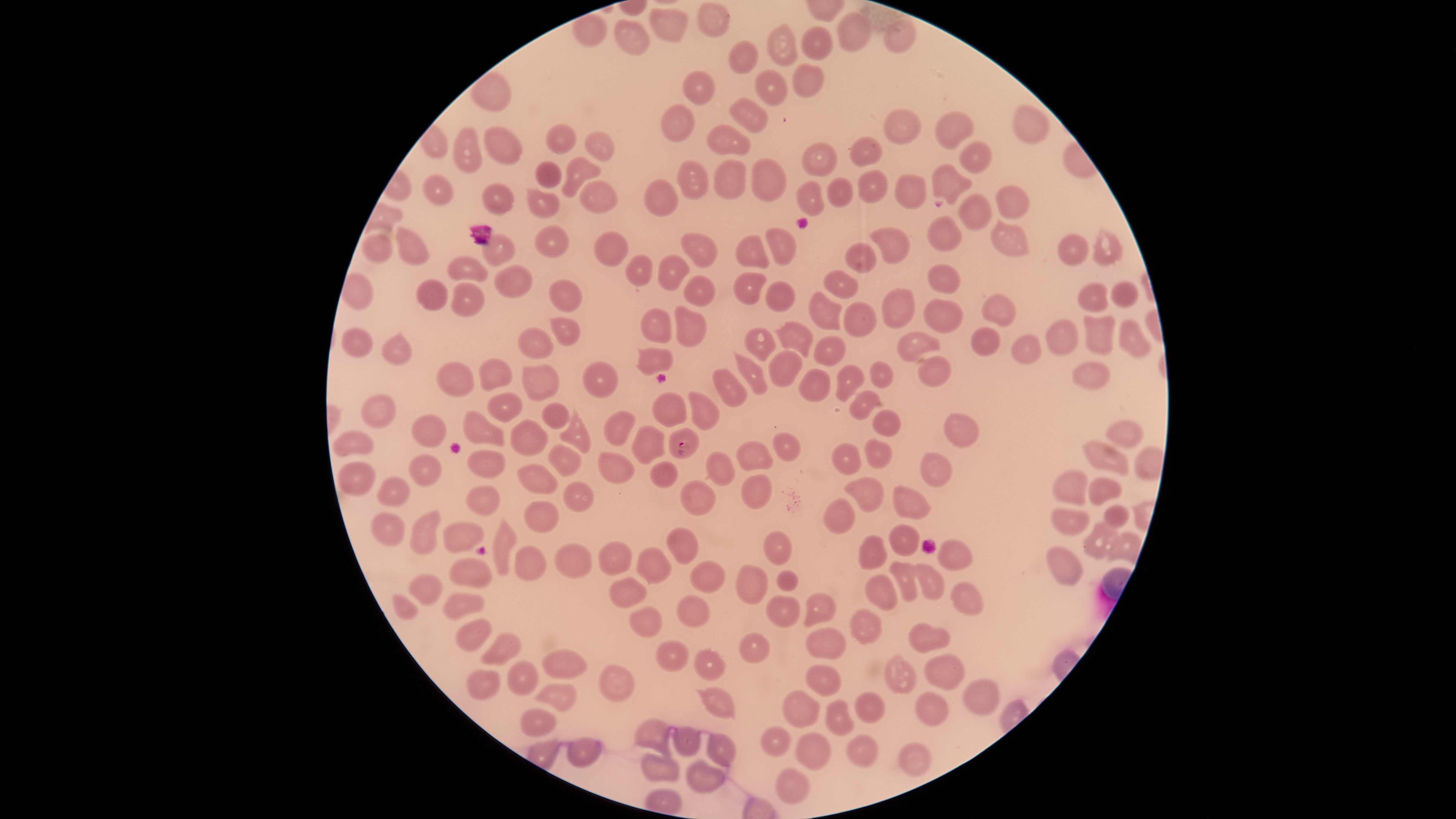

Approximate bounding boxes, in pixels from the top-left corner.
Summary:
  - Uninfected red blood cells: (left=696, top=1, right=732, bottom=41), (left=648, top=6, right=688, bottom=44), (left=835, top=11, right=872, bottom=52), (left=614, top=16, right=651, bottom=57), (left=882, top=18, right=917, bottom=55), (left=765, top=23, right=799, bottom=69), (left=801, top=23, right=833, bottom=61), (left=728, top=40, right=760, bottom=74), (left=792, top=63, right=825, bottom=98), (left=754, top=68, right=788, bottom=106), (left=683, top=70, right=716, bottom=105), (left=728, top=96, right=769, bottom=133), (left=660, top=103, right=695, bottom=143), (left=1010, top=103, right=1051, bottom=146), (left=882, top=108, right=922, bottom=146), (left=934, top=109, right=975, bottom=151), (left=545, top=122, right=577, bottom=156), (left=706, top=122, right=751, bottom=157), (left=483, top=126, right=524, bottom=167), (left=453, top=127, right=483, bottom=174), (left=583, top=128, right=616, bottom=164), (left=849, top=136, right=883, bottom=166), (left=959, top=140, right=993, bottom=175), (left=801, top=143, right=839, bottom=179), (left=561, top=155, right=602, bottom=199), (left=750, top=158, right=788, bottom=204), (left=712, top=159, right=748, bottom=200), (left=534, top=160, right=563, bottom=188), (left=676, top=160, right=709, bottom=201), (left=930, top=162, right=974, bottom=206), (left=857, top=169, right=889, bottom=203), (left=422, top=173, right=454, bottom=207), (left=895, top=173, right=927, bottom=210), (left=826, top=176, right=854, bottom=207), (left=644, top=178, right=679, bottom=217), (left=579, top=180, right=619, bottom=214), (left=795, top=180, right=824, bottom=217), (left=481, top=182, right=516, bottom=217), (left=995, top=184, right=1030, bottom=221), (left=524, top=186, right=561, bottom=218), (left=957, top=193, right=993, bottom=232), (left=927, top=216, right=963, bottom=253), (left=990, top=218, right=1031, bottom=259), (left=394, top=224, right=431, bottom=267), (left=534, top=224, right=570, bottom=259), (left=765, top=226, right=798, bottom=267), (left=869, top=226, right=910, bottom=266), (left=1092, top=227, right=1121, bottom=266), (left=593, top=230, right=630, bottom=267), (left=362, top=232, right=394, bottom=266), (left=681, top=232, right=718, bottom=269), (left=1057, top=232, right=1090, bottom=267), (left=480, top=234, right=517, bottom=267), (left=734, top=234, right=769, bottom=269), (left=843, top=242, right=878, bottom=274), (left=447, top=254, right=488, bottom=283), (left=625, top=254, right=654, bottom=288), (left=657, top=254, right=690, bottom=292), (left=493, top=263, right=533, bottom=299), (left=927, top=263, right=962, bottom=296), (left=732, top=270, right=768, bottom=305), (left=822, top=270, right=859, bottom=300), (left=683, top=274, right=716, bottom=307), (left=416, top=276, right=450, bottom=312), (left=549, top=279, right=584, bottom=313), (left=450, top=280, right=486, bottom=319), (left=765, top=280, right=797, bottom=312), (left=1110, top=280, right=1139, bottom=308), (left=1077, top=282, right=1108, bottom=314), (left=881, top=287, right=916, bottom=328), (left=808, top=290, right=842, bottom=331), (left=980, top=292, right=1016, bottom=328), (left=923, top=299, right=963, bottom=334), (left=843, top=301, right=877, bottom=339), (left=674, top=304, right=708, bottom=348), (left=639, top=306, right=673, bottom=344), (left=1082, top=313, right=1117, bottom=358), (left=548, top=316, right=581, bottom=348), (left=1045, top=318, right=1079, bottom=356), (left=1117, top=318, right=1152, bottom=360), (left=772, top=320, right=815, bottom=358), (left=517, top=325, right=555, bottom=359), (left=341, top=326, right=374, bottom=358), (left=743, top=326, right=777, bottom=362), (left=970, top=326, right=1001, bottom=357), (left=380, top=329, right=412, bottom=367), (left=896, top=331, right=942, bottom=364), (left=1011, top=334, right=1042, bottom=366), (left=812, top=335, right=846, bottom=367), (left=634, top=347, right=673, bottom=376), (left=768, top=349, right=803, bottom=389), (left=734, top=351, right=770, bottom=397), (left=916, top=355, right=951, bottom=388), (left=477, top=358, right=512, bottom=392), (left=869, top=358, right=894, bottom=389), (left=581, top=360, right=618, bottom=398), (left=1072, top=360, right=1110, bottom=391), (left=434, top=361, right=475, bottom=399), (left=522, top=363, right=561, bottom=402), (left=835, top=363, right=865, bottom=403), (left=711, top=367, right=748, bottom=408), (left=798, top=368, right=832, bottom=404), (left=848, top=389, right=882, bottom=420), (left=687, top=390, right=720, bottom=432), (left=486, top=391, right=523, bottom=424), (left=651, top=391, right=687, bottom=428), (left=361, top=393, right=397, bottom=429), (left=541, top=401, right=570, bottom=430), (left=559, top=404, right=592, bottom=454), (left=602, top=408, right=636, bottom=446), (left=463, top=409, right=506, bottom=447), (left=872, top=409, right=902, bottom=438), (left=944, top=413, right=980, bottom=448), (left=411, top=414, right=449, bottom=448), (left=509, top=417, right=549, bottom=457), (left=1104, top=420, right=1145, bottom=449), (left=631, top=424, right=666, bottom=465), (left=332, top=429, right=376, bottom=459), (left=771, top=432, right=802, bottom=462), (left=864, top=436, right=894, bottom=469), (left=1082, top=439, right=1129, bottom=476), (left=735, top=440, right=774, bottom=473), (left=831, top=442, right=862, bottom=476), (left=546, top=443, right=583, bottom=478), (left=1133, top=445, right=1165, bottom=482), (left=468, top=448, right=506, bottom=479), (left=597, top=450, right=637, bottom=486), (left=705, top=451, right=737, bottom=486), (left=918, top=452, right=954, bottom=488), (left=408, top=453, right=443, bottom=487), (left=338, top=460, right=376, bottom=496), (left=516, top=462, right=559, bottom=495), (left=650, top=462, right=677, bottom=488), (left=1052, top=470, right=1088, bottom=506), (left=740, top=474, right=773, bottom=510), (left=843, top=475, right=887, bottom=513), (left=376, top=476, right=410, bottom=507), (left=1087, top=477, right=1122, bottom=507), (left=562, top=479, right=595, bottom=513), (left=679, top=479, right=717, bottom=517), (left=892, top=483, right=933, bottom=521), (left=465, top=484, right=500, bottom=519), (left=823, top=496, right=856, bottom=535), (left=523, top=500, right=561, bottom=534), (left=1103, top=503, right=1130, bottom=529), (left=1050, top=507, right=1091, bottom=536), (left=407, top=508, right=443, bottom=557), (left=370, top=512, right=407, bottom=548), (left=491, top=515, right=519, bottom=577), (left=1081, top=520, right=1119, bottom=560), (left=443, top=521, right=485, bottom=555), (left=888, top=523, right=921, bottom=556), (left=665, top=525, right=699, bottom=565), (left=763, top=529, right=793, bottom=567), (left=1107, top=530, right=1143, bottom=567), (left=857, top=534, right=888, bottom=572), (left=938, top=538, right=973, bottom=571), (left=597, top=541, right=633, bottom=576), (left=553, top=542, right=594, bottom=579), (left=514, top=545, right=547, bottom=582), (left=1046, top=545, right=1085, bottom=586), (left=635, top=546, right=673, bottom=585), (left=448, top=557, right=493, bottom=589), (left=689, top=560, right=726, bottom=594), (left=888, top=560, right=919, bottom=602), (left=911, top=562, right=945, bottom=600), (left=735, top=564, right=769, bottom=605), (left=776, top=569, right=800, bottom=592), (left=408, top=572, right=444, bottom=607), (left=865, top=574, right=898, bottom=611), (left=609, top=576, right=647, bottom=609), (left=950, top=581, right=984, bottom=616), (left=803, top=591, right=836, bottom=627), (left=391, top=593, right=419, bottom=620), (left=442, top=593, right=485, bottom=622), (left=676, top=593, right=709, bottom=628), (left=765, top=593, right=802, bottom=627), (left=628, top=605, right=663, bottom=638), (left=850, top=607, right=883, bottom=645), (left=454, top=617, right=493, bottom=653), (left=908, top=621, right=953, bottom=654), (left=805, top=626, right=848, bottom=661), (left=480, top=632, right=524, bottom=666), (left=738, top=632, right=773, bottom=664), (left=655, top=640, right=690, bottom=672), (left=693, top=648, right=726, bottom=681), (left=542, top=649, right=588, bottom=680), (left=885, top=651, right=918, bottom=696), (left=924, top=653, right=966, bottom=692), (left=507, top=661, right=539, bottom=696), (left=804, top=663, right=842, bottom=697), (left=598, top=664, right=635, bottom=703), (left=467, top=669, right=500, bottom=700), (left=962, top=677, right=1001, bottom=717), (left=534, top=682, right=577, bottom=714), (left=694, top=685, right=737, bottom=721), (left=781, top=689, right=821, bottom=730), (left=915, top=690, right=949, bottom=729), (left=854, top=691, right=886, bottom=725), (left=824, top=698, right=855, bottom=735), (left=520, top=707, right=557, bottom=738), (left=634, top=717, right=673, bottom=757), (left=673, top=725, right=702, bottom=757), (left=760, top=726, right=791, bottom=758), (left=795, top=731, right=833, bottom=772), (left=706, top=732, right=738, bottom=768), (left=847, top=733, right=880, bottom=769), (left=566, top=737, right=604, bottom=768), (left=898, top=742, right=933, bottom=779), (left=641, top=752, right=682, bottom=784), (left=685, top=757, right=726, bottom=795), (left=773, top=766, right=811, bottom=806)
  - Parasitized red blood cells: (left=669, top=426, right=700, bottom=460)
  - Visible region: circular
  - Species: Plasmodium falciparum
  - Presence: malaria parasites detected
  - Preparation: thin blood smear
  - Stain: Giemsa
  - Field of view: single
  - Capture: smartphone photograph through the microscope eyepiece
  - Image size: 1456×819 pixels